Classify the preparation.
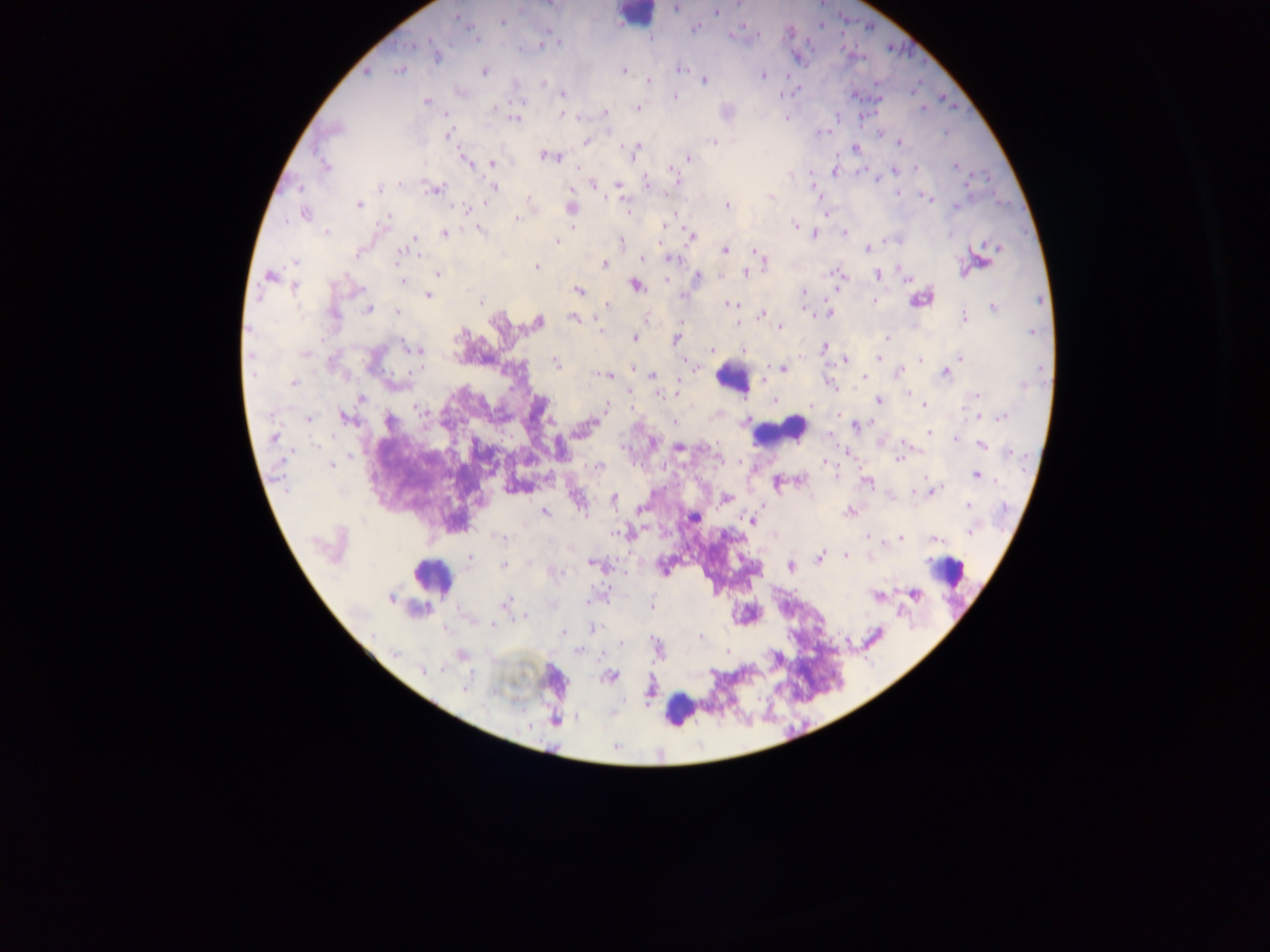

Thick blood smear.

Approximate centers as {x, y} in pixels.
Summary:
  - Malaria parasite locations: {677, 8}, {715, 12}, {502, 21}, {695, 28}, {730, 34}, {649, 38}, {560, 42}, {554, 43}, {542, 44}, {436, 56}, {797, 57}, {680, 68}, {399, 69}, {623, 70}, {366, 71}, {483, 71}, {763, 75}, {703, 80}, {648, 81}, {543, 82}, {561, 94}, {852, 94}, {674, 96}, {878, 97}, {426, 101}, {636, 107}, {605, 113}, {446, 114}, {561, 115}, {786, 117}, {516, 118}, {879, 133}, {448, 135}, {587, 141}, {713, 141}, {899, 143}, {854, 147}, {635, 148}, {548, 155}, {687, 158}, {465, 160}, {491, 163}, {954, 165}, {325, 167}, {917, 169}, {672, 170}, {894, 170}, {835, 171}, {676, 181}, {593, 183}, {400, 185}, {618, 185}, {646, 185}, {493, 187}, {299, 188}, {813, 188}, {434, 190}, {899, 192}, {529, 197}, {932, 199}, {358, 204}, {726, 205}, {570, 208}, {468, 209}, {827, 213}, {305, 214}, {516, 218}, {574, 225}, {663, 225}, {795, 225}, {479, 228}, {327, 232}, {843, 232}, {445, 233}, {814, 233}, {690, 236}, {415, 238}, {899, 240}, {622, 241}, {662, 241}, {557, 242}, {997, 247}, {866, 248}, {402, 250}, {724, 250}, {755, 251}, {640, 258}, {671, 258}, {763, 260}, {979, 263}, {604, 264}, {535, 267}, {745, 272}, {437, 273}, {838, 273}, {877, 274}, {270, 276}, {696, 277}, {906, 279}, {400, 280}, {666, 280}, {636, 284}, {295, 286}, {578, 289}, {837, 289}, {803, 292}, {428, 295}, {683, 298}, {921, 298}, {875, 300}, {479, 302}, {606, 305}, {728, 305}, {994, 308}, {368, 309}, {805, 309}, {397, 312}, {829, 313}, {334, 314}, {761, 314}, {574, 317}, {963, 317}, {646, 319}, {538, 322}, {738, 323}, {779, 327}, {884, 337}, {676, 338}, {634, 339}, {413, 348}, {824, 348}, {743, 349}, {712, 350}, {878, 358}, {960, 358}, {844, 360}, {920, 360}, {687, 362}, {556, 365}, {633, 368}, {782, 368}, {899, 371}, {946, 372}, {606, 374}, {652, 375}, {862, 376}, {294, 384}, {677, 392}, {629, 393}, {908, 394}, {975, 395}, {361, 399}, {772, 400}, {878, 401}, {812, 405}, {924, 405}, {605, 407}, {630, 408}, {837, 415}, {1001, 416}, {345, 417}, {979, 417}, {309, 419}, {745, 420}, {389, 423}, {673, 423}, {855, 425}, {581, 430}, {929, 432}, {829, 435}, {274, 437}, {955, 438}, {652, 443}, {981, 445}, {679, 449}, {846, 453}, {898, 458}, {741, 463}, {823, 464}, {331, 465}, {598, 467}, {975, 475}, {799, 481}, {867, 481}, {777, 482}, {913, 491}, {933, 491}, {613, 498}, {726, 498}, {968, 505}, {639, 509}, {544, 511}, {850, 511}, {693, 517}, {751, 520}, {631, 531}, {970, 532}, {613, 533}, {869, 537}, {500, 538}, {900, 538}, {934, 538}, {874, 540}, {884, 543}, {334, 545}, {845, 555}, {819, 557}, {870, 557}, {470, 558}, {591, 562}, {502, 566}, {790, 566}, {662, 568}, {913, 593}, {877, 596}, {390, 598}, {505, 603}, {651, 606}, {525, 616}, {493, 623}, {591, 628}, {563, 633}, {701, 637}, {620, 644}, {656, 646}, {577, 650}, {461, 655}, {424, 670}, {611, 676}, {464, 688}, {648, 692}
  - Leukocyte locations: {634, 16}, {733, 378}, {780, 430}, {949, 571}, {432, 577}, {679, 710}
  - Image size: 1270×952 pixels
  - Country: Ghana
  - Field of view: single
  - Capture: mobile-phone photograph through a microscope